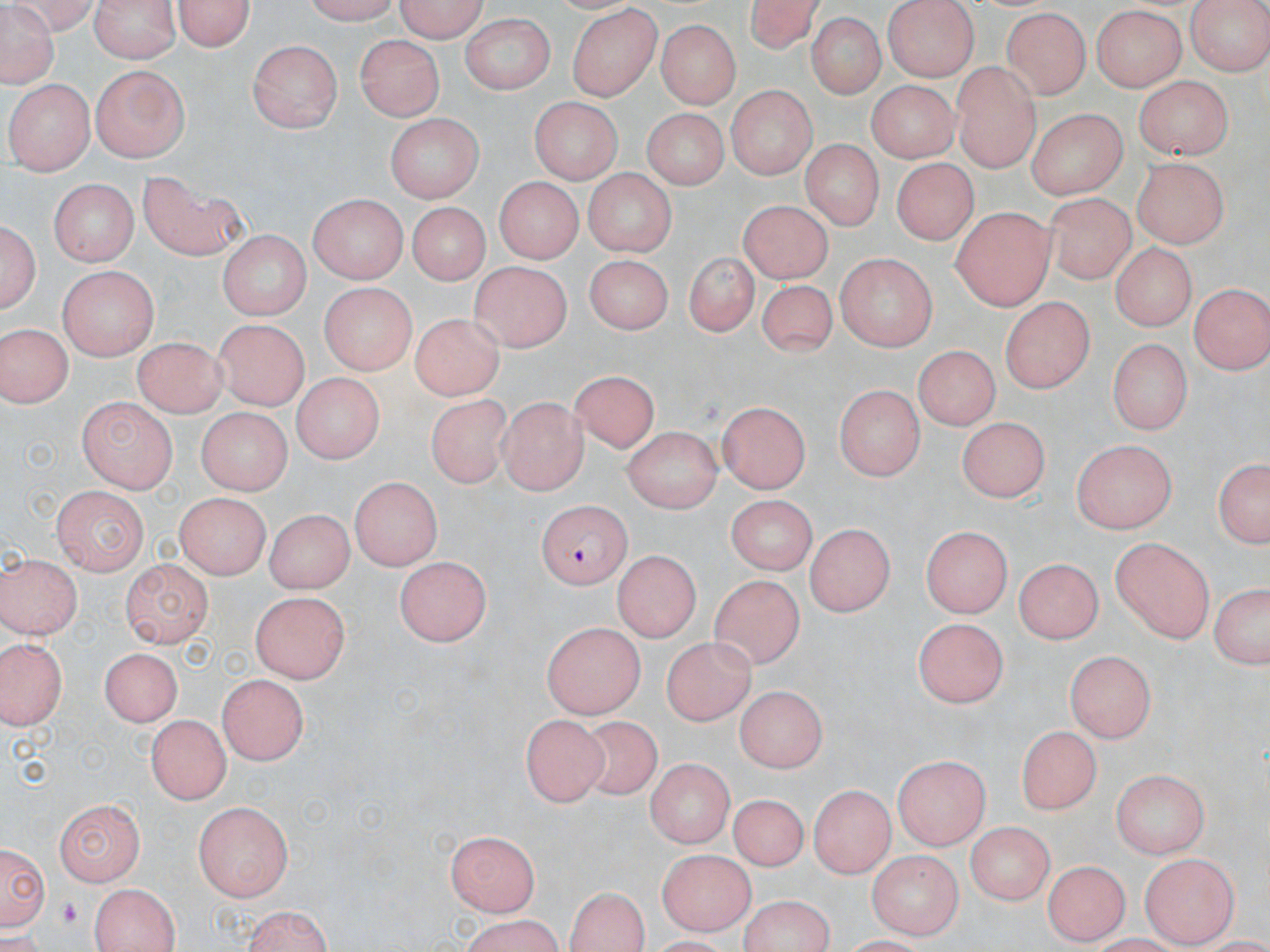

slide-level diagnosis = Plasmodium falciparum
image size = 1270×952 pixels
uninfected red blood cell locations = approximate bounding boxes as (x1, y1, x2, y2) in pixels: (5, 0, 99, 35), (90, 0, 181, 61), (300, 0, 408, 23), (396, 0, 490, 42), (742, 0, 825, 55), (882, 0, 976, 80), (1184, 0, 1270, 75), (171, 1, 257, 53), (0, 2, 60, 89), (1088, 6, 1186, 92), (566, 8, 661, 102), (1000, 9, 1094, 99), (461, 12, 557, 97), (806, 14, 884, 100), (657, 19, 742, 108), (356, 36, 446, 120), (247, 39, 339, 132), (952, 60, 1042, 170), (90, 64, 190, 163), (1133, 74, 1230, 161), (867, 78, 958, 161), (8, 79, 94, 174), (725, 85, 813, 178), (532, 97, 621, 185), (1027, 105, 1130, 200), (639, 108, 728, 191), (384, 114, 485, 199), (804, 143, 880, 227), (895, 160, 974, 244), (1133, 160, 1226, 248), (581, 168, 676, 258), (138, 169, 250, 260), (494, 174, 586, 262), (50, 177, 138, 265), (1042, 192, 1133, 285), (305, 194, 410, 284), (737, 200, 833, 280), (402, 201, 492, 288), (948, 209, 1054, 310), (2, 218, 40, 318), (216, 231, 308, 321), (1111, 242, 1196, 331), (686, 247, 757, 335), (834, 253, 942, 346), (583, 254, 671, 336), (469, 260, 573, 352), (58, 265, 157, 361), (757, 277, 835, 359), (1189, 283, 1268, 374), (320, 284, 412, 376), (998, 295, 1098, 394), (406, 317, 502, 401), (211, 320, 311, 407), (0, 323, 69, 407), (131, 333, 226, 417), (1108, 337, 1192, 437), (911, 346, 999, 430), (568, 371, 657, 454), (289, 374, 383, 462), (833, 384, 925, 481), (429, 394, 519, 489), (76, 395, 178, 491), (497, 397, 588, 493), (718, 401, 812, 492), (194, 407, 290, 494), (952, 414, 1045, 500), (622, 426, 719, 512), (1073, 439, 1174, 535), (1211, 455, 1269, 554), (348, 474, 443, 572), (50, 485, 147, 573), (175, 492, 275, 578), (723, 493, 812, 571), (265, 505, 352, 595), (803, 524, 897, 613), (923, 524, 1013, 616), (1108, 537, 1215, 642), (612, 548, 698, 643), (1, 554, 79, 642), (395, 554, 491, 644), (1013, 558, 1102, 644), (120, 559, 213, 645), (710, 573, 806, 668), (1205, 581, 1270, 671), (251, 591, 352, 683), (912, 618, 1009, 709), (542, 622, 646, 718), (0, 636, 71, 727), (659, 638, 757, 723), (1065, 643, 1156, 741), (100, 647, 184, 730), (215, 674, 312, 766), (735, 687, 830, 768), (146, 713, 234, 802), (521, 714, 608, 804), (580, 715, 664, 803), (1018, 724, 1100, 815), (893, 754, 988, 849), (647, 757, 733, 851), (1113, 769, 1213, 860), (808, 783, 894, 877), (730, 792, 804, 874), (51, 799, 148, 885), (193, 801, 293, 903), (966, 821, 1053, 904), (447, 833, 544, 917), (2, 837, 50, 935), (655, 848, 751, 935), (867, 849, 962, 936), (1142, 854, 1235, 945), (1045, 858, 1129, 945), (89, 883, 179, 952), (562, 886, 652, 951), (733, 896, 842, 952), (237, 905, 339, 952), (453, 918, 569, 952)
preparation = thin blood film
modality = optical microscopy
Plasmodium falciparum-infected red blood cell locations = approximate bounding boxes as (x1, y1, x2, y2) in pixels: (539, 502, 631, 591)
field of view = single
platelet locations = approximate bounding boxes as (x1, y1, x2, y2) in pixels: (57, 897, 81, 926)
stain = May-Grünwald-Giemsa
magnification = 1000x